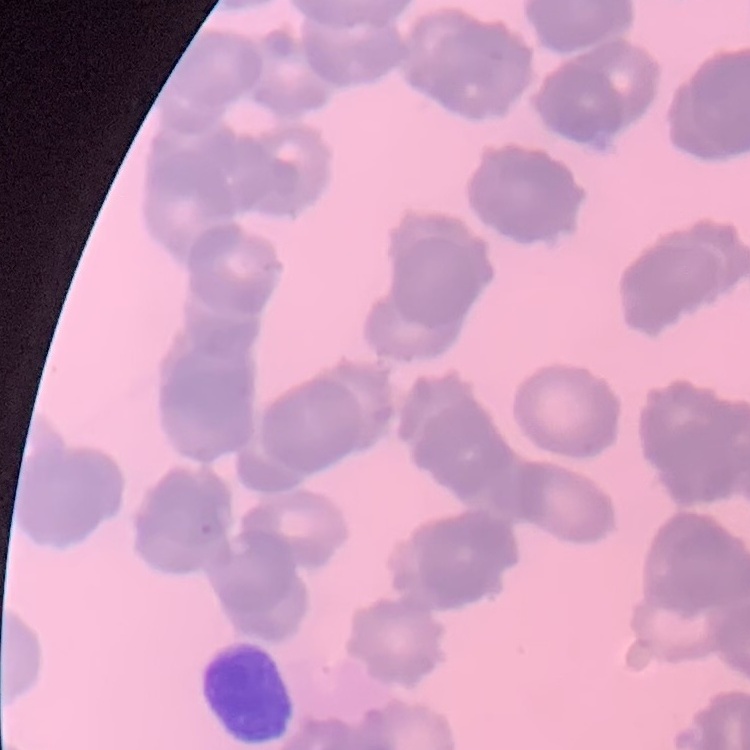 The red blood cells show rouleaux formation. Thin blood smear. Field's or Giemsa stain. Square crop of a larger photomicrograph.